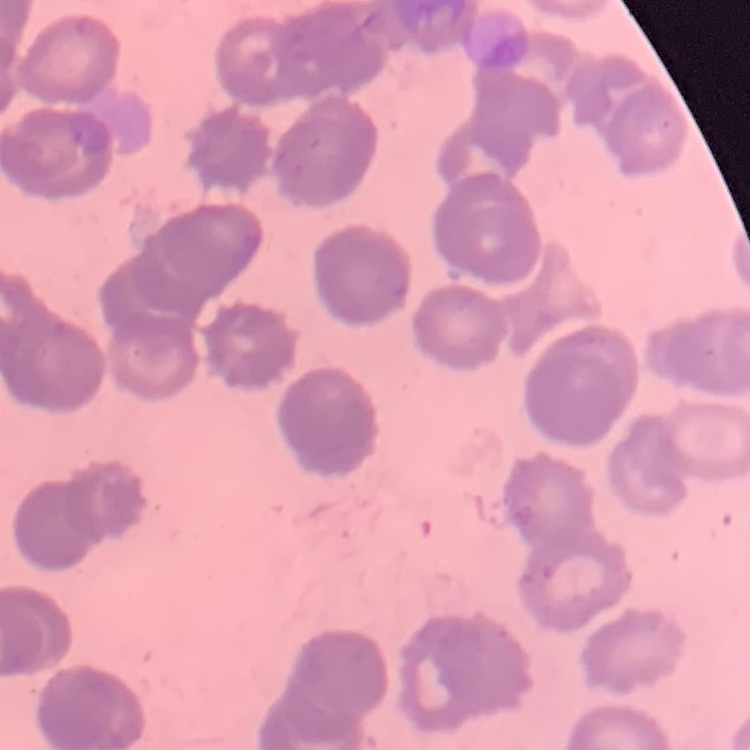
Summary:
  - Erythrocyte morphology: rouleaux formation
  - Image type: one tile cut from a larger photomicrograph
  - Stain: Field's or Giemsa
  - Preparation: thin peripheral smear